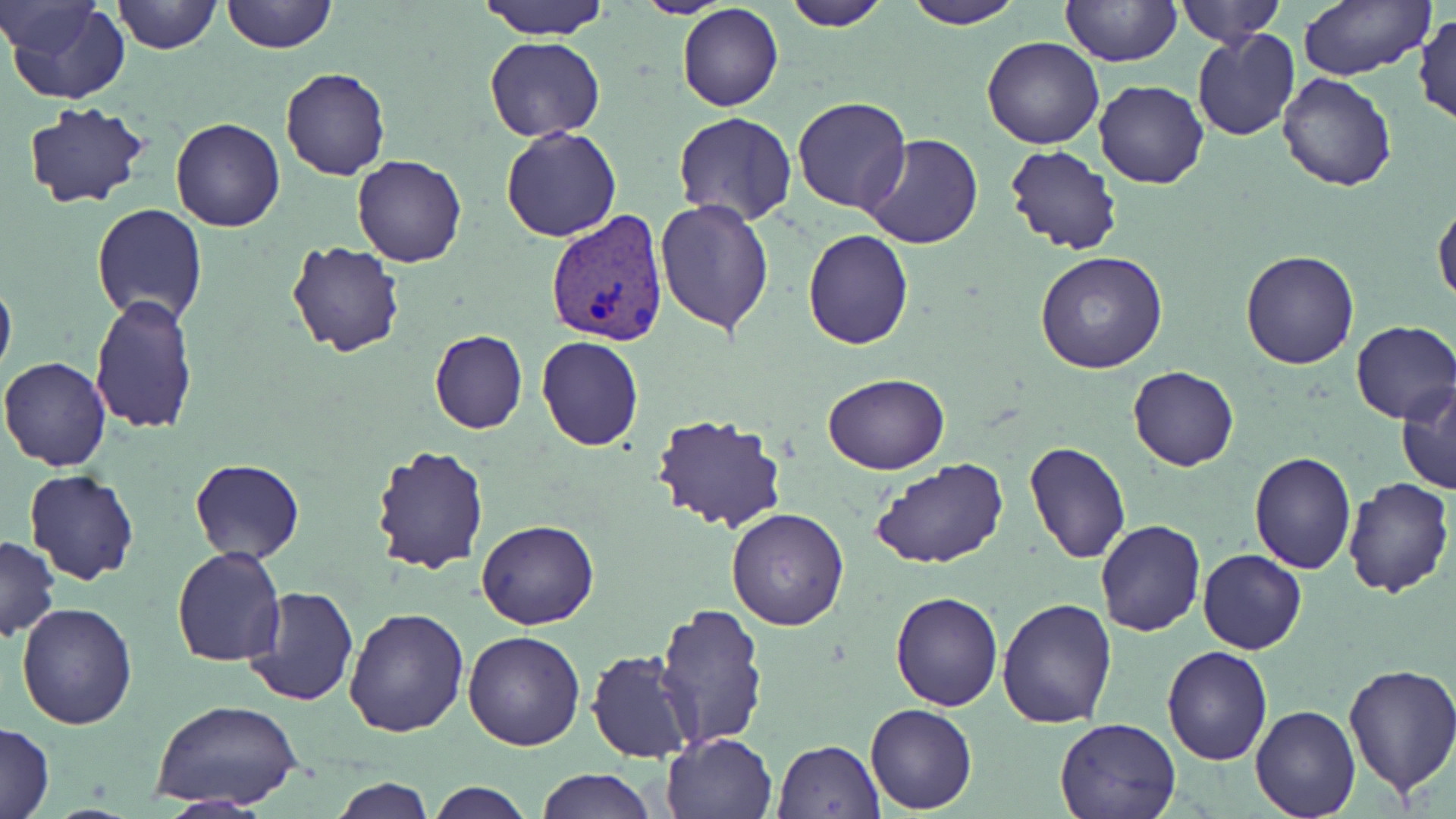
Approximate bounding boxes as [x1, y1, x2, y2] in pixels. Plasmodium vivax-infected red blood cell locations: [545, 209, 672, 347]. Uninfected red blood cell locations: [1, 0, 101, 57], [222, 0, 335, 53], [478, 0, 610, 40], [634, 0, 730, 19], [784, 0, 891, 30], [900, 0, 1020, 29], [1176, 0, 1285, 48], [4, 1, 132, 105], [112, 1, 222, 54], [1061, 1, 1181, 67], [1295, 1, 1434, 81], [678, 5, 783, 111], [1414, 11, 1456, 129], [1191, 30, 1300, 143], [484, 36, 607, 142], [981, 36, 1105, 149], [281, 69, 390, 180], [1277, 71, 1398, 192], [1093, 79, 1209, 189], [792, 96, 911, 213], [21, 101, 151, 208], [673, 110, 799, 226], [171, 117, 285, 232], [501, 126, 621, 242], [858, 133, 984, 251], [1004, 144, 1125, 257], [352, 154, 466, 268], [654, 199, 775, 336], [1433, 199, 1456, 310], [91, 203, 208, 327], [803, 227, 914, 349], [285, 241, 406, 357], [1241, 248, 1362, 369], [1035, 251, 1168, 374], [0, 274, 16, 383], [88, 293, 198, 435], [1350, 321, 1456, 424], [429, 329, 527, 434], [536, 336, 643, 452], [0, 355, 112, 472], [1128, 366, 1239, 472], [822, 374, 950, 473], [1397, 382, 1456, 497], [647, 413, 790, 534], [1022, 440, 1131, 565], [371, 445, 491, 575], [1248, 451, 1356, 575], [189, 458, 304, 563], [868, 459, 1010, 568], [24, 468, 141, 585], [1339, 478, 1455, 597], [725, 506, 850, 631], [477, 518, 599, 630], [1094, 520, 1206, 637], [0, 534, 60, 642], [171, 546, 286, 666], [1198, 549, 1306, 654], [241, 585, 360, 708], [890, 590, 1003, 710], [995, 598, 1117, 729], [17, 603, 137, 729], [653, 604, 770, 747], [343, 605, 470, 738], [463, 631, 584, 751], [1161, 645, 1273, 765], [586, 650, 698, 763], [1341, 664, 1456, 796], [1252, 684, 1451, 808], [153, 698, 302, 814], [1250, 703, 1361, 819], [865, 704, 977, 814], [1054, 714, 1182, 819], [1, 722, 54, 819], [661, 731, 777, 819], [772, 739, 886, 818], [534, 768, 654, 819], [330, 777, 433, 818], [426, 781, 535, 819], [155, 795, 277, 818]. Slide-level diagnosis: Plasmodium vivax. Captured at 1000x magnification. Thin blood film. One field of a larger specimen. Optical microscopy. Image is 1456×819 pixels. May-Grünwald-Giemsa stain.